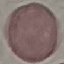
Summary:
  - Malaria status: uninfected
  - Capture: smartphone through the microscope eyepiece
  - Preparation: thin blood film
  - Image type: automatically extracted cell patch, resized to 64 × 64 pixels
  - Stain: Giemsa